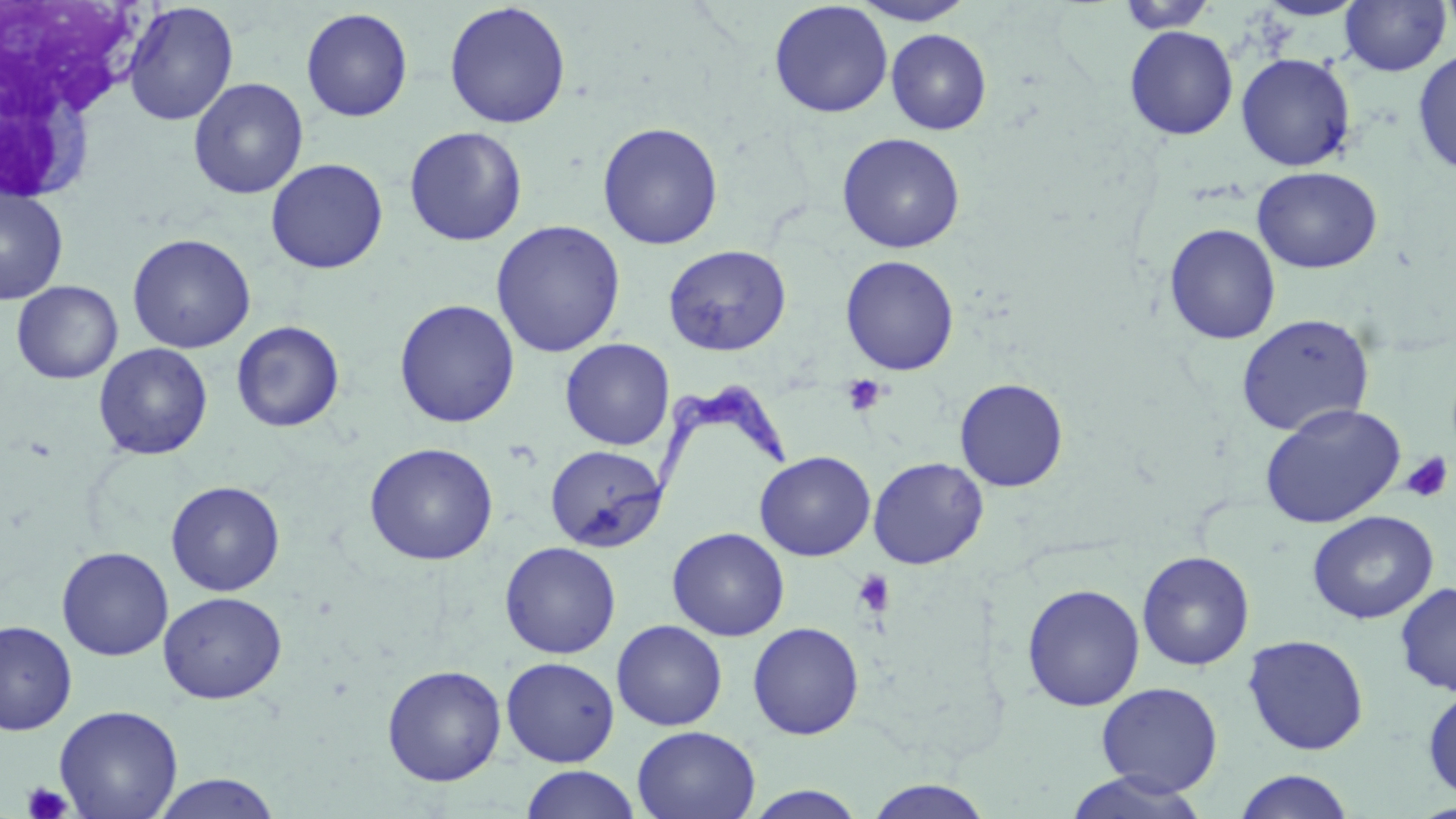
Approximate bounding boxes as [x1, y1, x2, y2] in pixels. Trypanosoma brucei locations: [608, 374, 792, 518]. Uninfected red blood cell locations: [851, 0, 976, 26], [1254, 0, 1368, 21], [1437, 0, 1456, 43], [769, 1, 893, 118], [1116, 1, 1219, 33], [1339, 1, 1451, 76], [122, 2, 239, 125], [443, 2, 571, 128], [301, 7, 413, 122], [1125, 26, 1239, 140], [886, 29, 992, 135], [1412, 49, 1456, 176], [1236, 53, 1356, 171], [188, 77, 309, 199], [597, 121, 724, 250], [404, 126, 528, 246], [837, 132, 965, 253], [265, 158, 388, 273], [1252, 166, 1382, 273], [0, 186, 69, 304], [490, 220, 626, 358], [1163, 223, 1281, 345], [127, 233, 255, 353], [663, 245, 791, 356], [840, 255, 960, 375], [11, 280, 123, 384], [394, 299, 521, 428], [1235, 313, 1375, 436], [231, 321, 345, 433], [559, 338, 675, 450], [93, 342, 213, 461], [954, 378, 1069, 491], [1260, 404, 1406, 528], [364, 442, 499, 565], [545, 445, 668, 552], [755, 451, 876, 561], [868, 457, 988, 570], [166, 480, 285, 596], [1307, 510, 1438, 624], [667, 527, 790, 641], [499, 541, 621, 658], [56, 546, 174, 661], [1136, 550, 1255, 671], [1395, 582, 1456, 697], [1022, 583, 1145, 711], [158, 591, 287, 704], [611, 619, 728, 731], [1, 620, 77, 735], [747, 621, 865, 740], [1242, 634, 1369, 755], [501, 656, 620, 766], [381, 664, 507, 786], [1095, 682, 1223, 796], [1422, 686, 1456, 801], [54, 705, 184, 819], [632, 726, 761, 819], [519, 765, 642, 818], [1233, 770, 1356, 819], [1064, 771, 1211, 819], [148, 772, 284, 818], [861, 779, 997, 819], [742, 785, 869, 818]. Platelet locations: [840, 374, 887, 416], [1400, 453, 1453, 504], [852, 569, 896, 619], [21, 781, 74, 819]. Slide-level diagnosis: Trypanosoma brucei. Thin blood film. Captured at 1000x magnification. Optical microscopy. May-Grünwald-Giemsa-stained preparation. One field of a larger specimen. Image is 1456×819 pixels.